Identify the parasite.
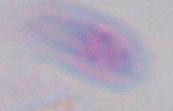
Toxoplasma gondii.

1000x magnification. Micrograph.